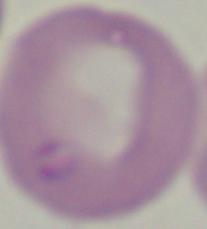
modality = micrograph
magnification = 1000x
identification = Babesia